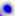

modality = micrograph
magnification = 400x
identification = Toxoplasma gondii